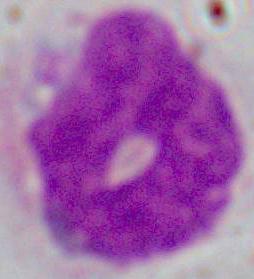
magnification = 1000x
identification = white blood cell
modality = micrograph